Locate every uninfected red blood cell.
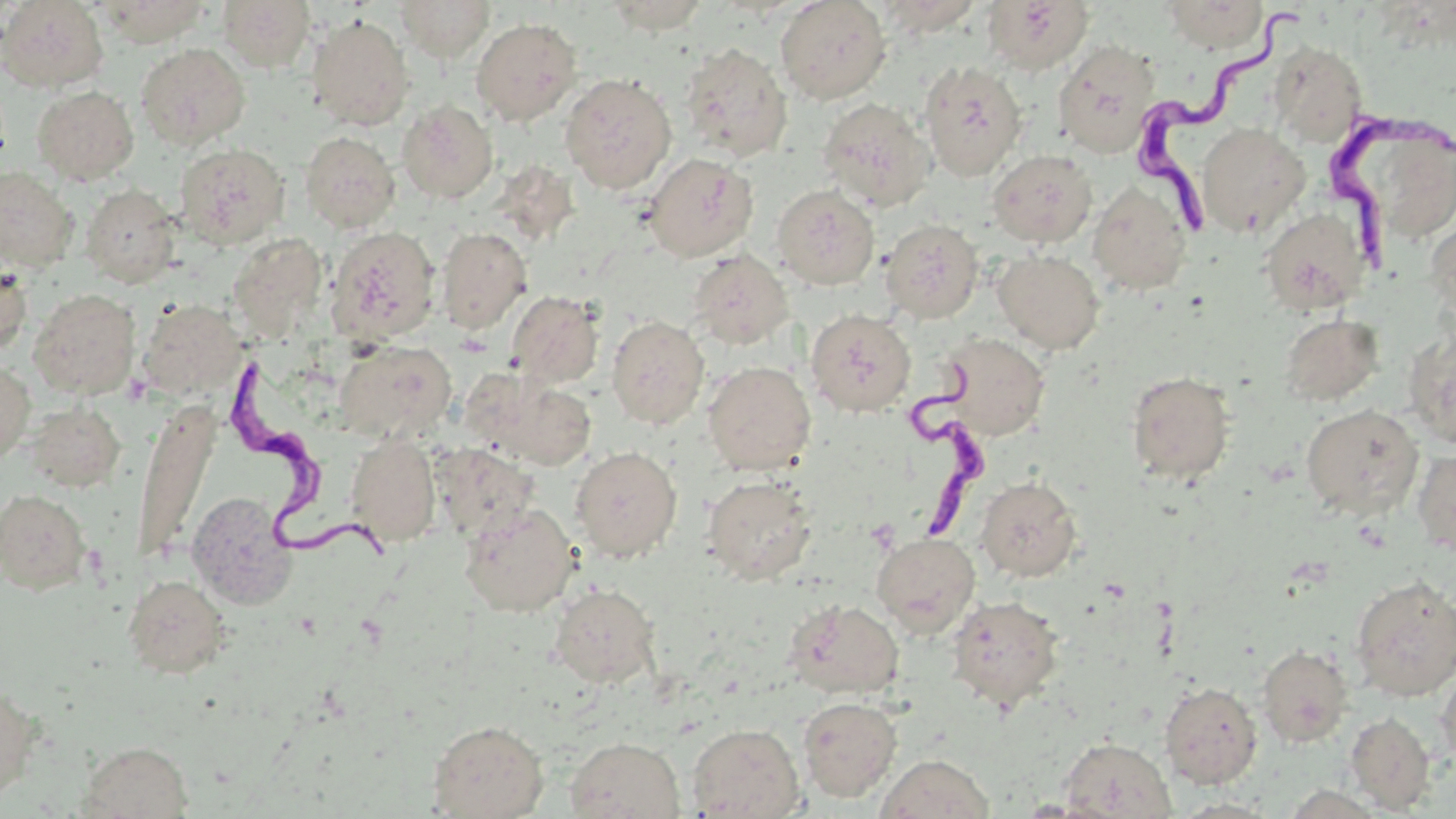
Approximate bounding boxes as named x1/y1/x2/y2 corners in pixels.
Uninfected red blood cells: (x1=0, y1=0, x2=109, y2=92), (x1=216, y1=0, x2=316, y2=72), (x1=395, y1=0, x2=495, y2=60), (x1=603, y1=0, x2=712, y2=33), (x1=776, y1=0, x2=891, y2=103), (x1=876, y1=0, x2=984, y2=35), (x1=1162, y1=0, x2=1268, y2=52), (x1=94, y1=1, x2=211, y2=46), (x1=983, y1=1, x2=1094, y2=74), (x1=308, y1=15, x2=414, y2=130), (x1=471, y1=17, x2=582, y2=125), (x1=1053, y1=39, x2=1161, y2=158), (x1=1268, y1=41, x2=1367, y2=146), (x1=136, y1=43, x2=250, y2=150), (x1=679, y1=43, x2=792, y2=161), (x1=918, y1=61, x2=1028, y2=181), (x1=560, y1=72, x2=677, y2=194), (x1=32, y1=85, x2=139, y2=185), (x1=817, y1=98, x2=934, y2=211), (x1=398, y1=100, x2=498, y2=203), (x1=1197, y1=123, x2=1309, y2=236), (x1=300, y1=131, x2=400, y2=233), (x1=1363, y1=132, x2=1456, y2=235), (x1=174, y1=143, x2=290, y2=248), (x1=988, y1=149, x2=1097, y2=248), (x1=644, y1=152, x2=758, y2=262), (x1=0, y1=166, x2=78, y2=272), (x1=1088, y1=181, x2=1193, y2=295), (x1=80, y1=184, x2=181, y2=288), (x1=772, y1=185, x2=880, y2=290), (x1=1260, y1=207, x2=1371, y2=315), (x1=1427, y1=216, x2=1456, y2=323), (x1=881, y1=219, x2=984, y2=323), (x1=327, y1=225, x2=441, y2=345), (x1=437, y1=226, x2=532, y2=334), (x1=228, y1=232, x2=328, y2=338), (x1=688, y1=250, x2=794, y2=350), (x1=993, y1=250, x2=1105, y2=354), (x1=0, y1=261, x2=32, y2=356), (x1=28, y1=288, x2=140, y2=399), (x1=507, y1=290, x2=604, y2=388), (x1=136, y1=298, x2=246, y2=399), (x1=806, y1=309, x2=916, y2=416), (x1=1280, y1=314, x2=1384, y2=406), (x1=606, y1=315, x2=709, y2=429), (x1=1403, y1=328, x2=1456, y2=449), (x1=939, y1=333, x2=1050, y2=441), (x1=335, y1=340, x2=456, y2=443), (x1=0, y1=360, x2=35, y2=465), (x1=703, y1=361, x2=817, y2=475), (x1=1127, y1=371, x2=1235, y2=486), (x1=482, y1=375, x2=597, y2=470), (x1=132, y1=400, x2=217, y2=566), (x1=25, y1=401, x2=126, y2=491), (x1=1301, y1=403, x2=1423, y2=519), (x1=346, y1=433, x2=441, y2=546), (x1=431, y1=444, x2=538, y2=542), (x1=570, y1=445, x2=682, y2=562), (x1=1412, y1=448, x2=1456, y2=556), (x1=702, y1=475, x2=818, y2=585), (x1=977, y1=476, x2=1082, y2=581), (x1=0, y1=488, x2=92, y2=595), (x1=186, y1=491, x2=298, y2=609), (x1=459, y1=502, x2=579, y2=617), (x1=872, y1=532, x2=981, y2=637), (x1=122, y1=574, x2=231, y2=678), (x1=1350, y1=575, x2=1456, y2=701), (x1=548, y1=583, x2=661, y2=689), (x1=946, y1=595, x2=1064, y2=711), (x1=784, y1=599, x2=905, y2=699), (x1=1257, y1=644, x2=1353, y2=747), (x1=1435, y1=665, x2=1456, y2=775), (x1=0, y1=682, x2=43, y2=804), (x1=1160, y1=682, x2=1263, y2=788), (x1=798, y1=696, x2=902, y2=802), (x1=1345, y1=712, x2=1436, y2=813), (x1=427, y1=719, x2=549, y2=818), (x1=688, y1=723, x2=804, y2=818), (x1=565, y1=736, x2=685, y2=819), (x1=1058, y1=737, x2=1176, y2=818), (x1=79, y1=741, x2=194, y2=818), (x1=877, y1=754, x2=994, y2=818), (x1=1171, y1=797, x2=1282, y2=817).

slide-level diagnosis = Trypanosoma brucei
stain = May-Grünwald-Giemsa
modality = light microscopy
preparation = thin blood smear
magnification = 1000x
Trypanosoma brucei locations = approximate bounding boxes as named x1/y1/x2/y2 corners in pixels: (x1=1130, y1=7, x2=1303, y2=230), (x1=1322, y1=113, x2=1452, y2=271), (x1=898, y1=357, x2=995, y2=540), (x1=233, y1=364, x2=395, y2=565)
field of view = one of a larger specimen
image size = 1456×819 pixels